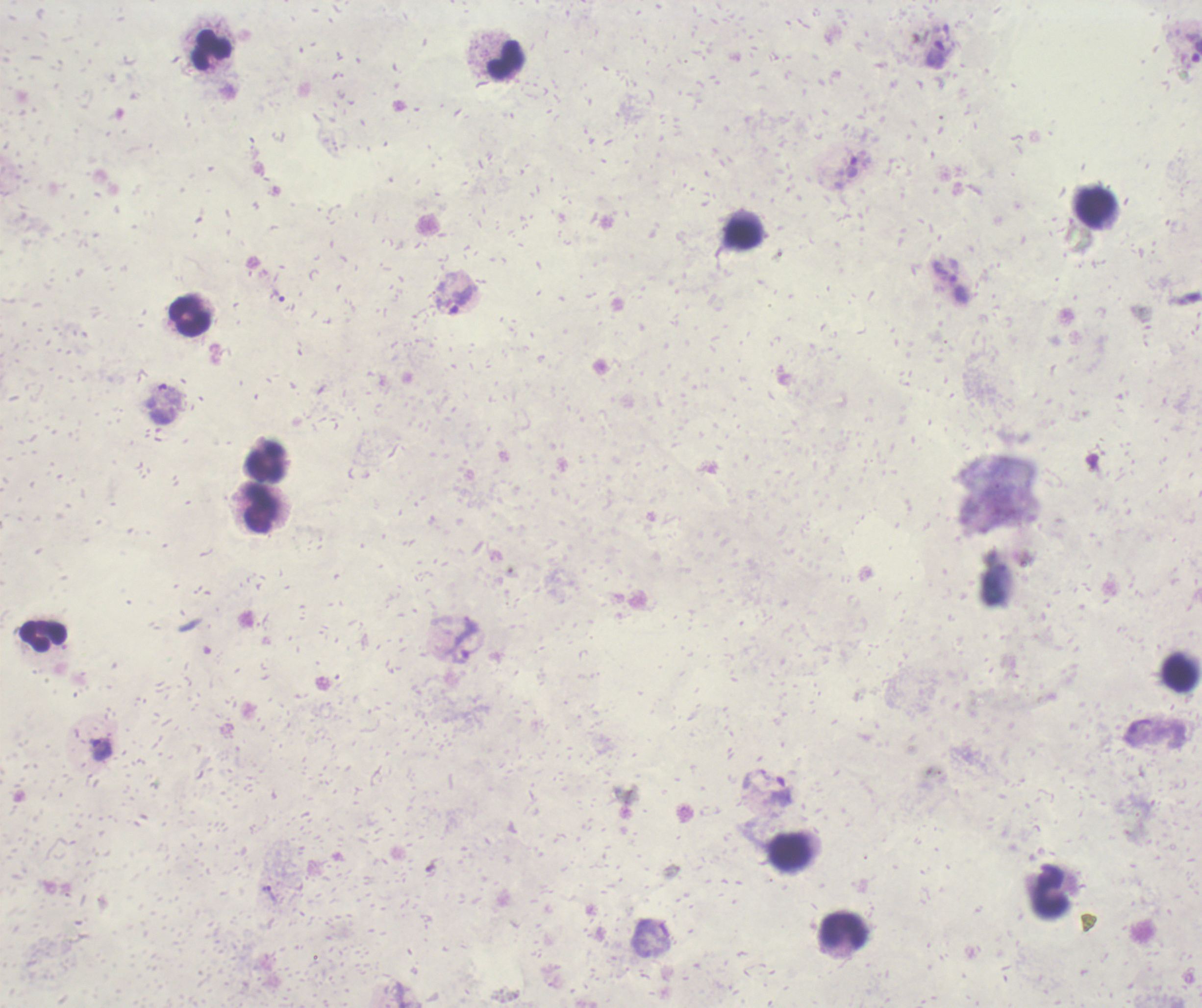
Approximate centers as (x, y) in pixels.
Summary:
  - Trophozoite locations: (937, 55), (851, 167), (279, 295), (462, 299), (467, 642), (102, 749), (780, 791), (271, 895)
  - Leukocyte locations: (212, 49), (506, 59), (1095, 207), (743, 235), (189, 317), (266, 462), (260, 508), (43, 636), (1179, 673), (790, 852), (1052, 893), (844, 931)
  - Magnification: 100x
  - Background quality: poor
  - Image size: 1202×1008 pixels
  - Stain: Romanowsky
  - Field of view: one from this slide
  - Result: positive for malaria parasites
  - Preparation: thick smear of blood
  - Coloration quality: bad
  - Context: previously used in a real diagnosis